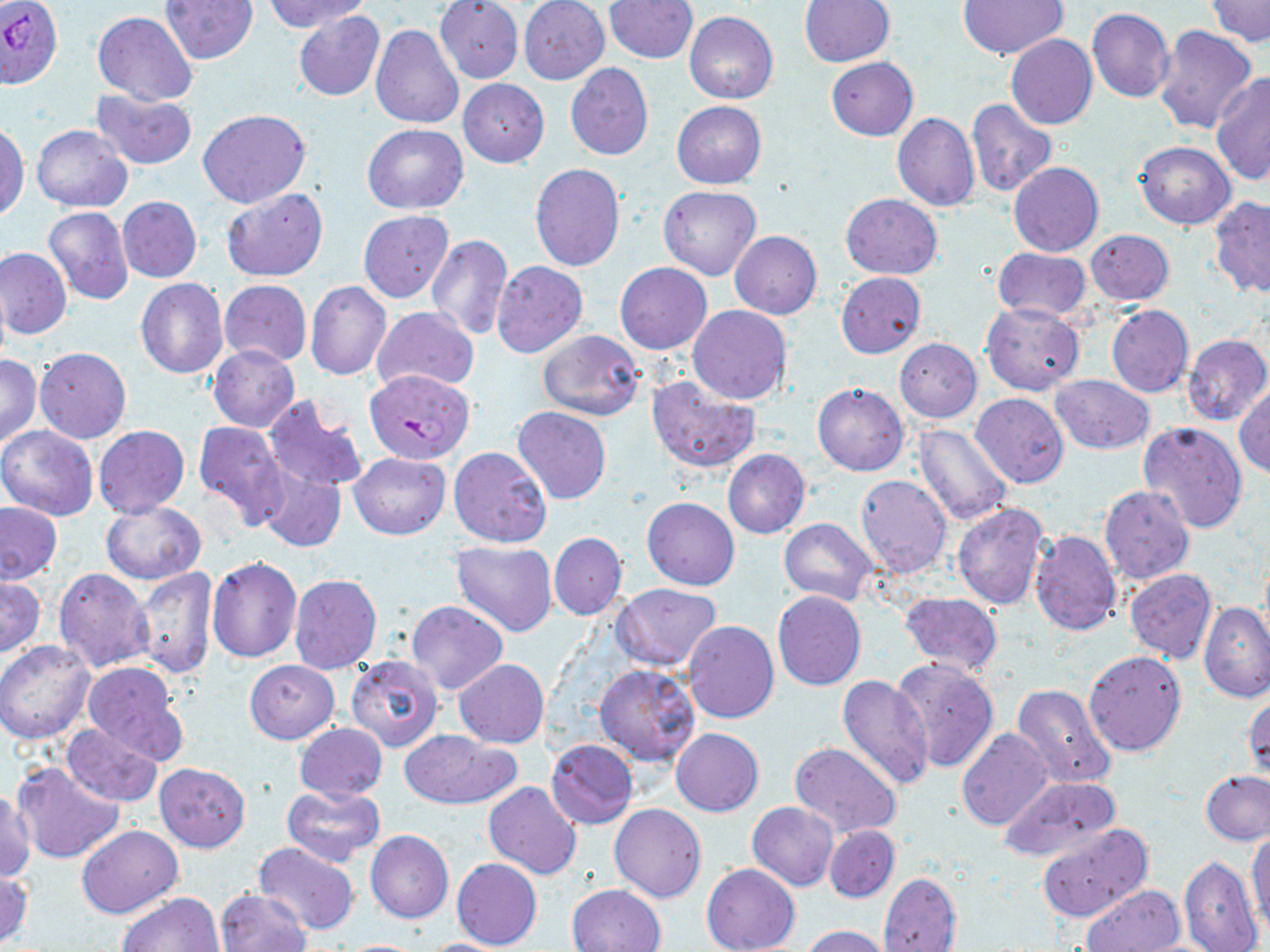 Approximate bounding boxes as (x1,y1)-(x2,y2) corner pairs in pixels. Uninfected red blood cell locations: (160,0)-(259,65), (605,0)-(698,63), (799,0)-(894,66), (1205,0)-(1270,46), (265,1)-(370,33), (518,1)-(609,85), (957,1)-(1067,59), (435,2)-(524,83), (1087,7)-(1175,103), (294,9)-(385,102), (92,12)-(197,105), (686,13)-(779,104), (371,25)-(463,127), (1154,25)-(1257,134), (1006,35)-(1097,130), (827,57)-(918,140), (565,63)-(653,161), (1211,73)-(1270,185), (458,79)-(550,167), (90,89)-(197,169), (966,100)-(1056,198), (672,101)-(765,188), (198,109)-(311,207), (893,112)-(979,212), (0,121)-(29,219), (31,124)-(132,212), (362,124)-(469,214), (1134,142)-(1235,229), (1009,163)-(1103,257), (530,164)-(625,271), (659,185)-(761,280), (221,187)-(328,281), (841,193)-(942,278), (118,196)-(202,282), (1210,196)-(1270,297), (43,207)-(134,306), (359,211)-(455,303), (729,230)-(822,319), (1085,230)-(1175,306), (426,235)-(514,342), (1,247)-(72,339), (993,247)-(1090,320), (492,260)-(588,359), (615,263)-(711,354), (836,271)-(926,358), (0,274)-(9,371), (137,278)-(228,378), (219,280)-(312,365), (305,280)-(392,380), (981,302)-(1085,395), (373,305)-(479,393), (687,305)-(791,404), (1106,305)-(1193,399), (537,329)-(644,422), (1182,334)-(1270,426), (895,338)-(982,422), (208,344)-(300,431), (36,347)-(130,444), (0,354)-(42,449), (1050,375)-(1154,454), (646,376)-(761,474), (813,383)-(909,476), (1235,385)-(1270,478), (972,392)-(1069,487), (263,396)-(366,496), (513,405)-(611,503), (194,420)-(288,526), (1138,421)-(1248,532), (911,423)-(1014,528), (93,425)-(189,518), (0,426)-(97,521), (449,446)-(552,547), (723,450)-(810,539), (349,452)-(451,539), (259,469)-(345,551), (855,475)-(953,578), (1100,485)-(1195,586), (643,497)-(740,590), (100,501)-(206,583), (0,502)-(63,584), (952,502)-(1050,611), (779,517)-(877,607), (1029,529)-(1122,636), (549,532)-(626,619), (450,542)-(558,637), (207,557)-(302,661), (131,566)-(218,680), (54,568)-(154,673), (1124,568)-(1217,663), (289,573)-(381,673), (0,576)-(45,658), (613,583)-(722,671), (772,590)-(867,690), (901,591)-(1003,675), (405,601)-(508,694), (1200,603)-(1270,701), (685,620)-(779,723), (1,640)-(96,744), (1084,651)-(1187,756), (345,655)-(443,753), (889,658)-(1000,775), (455,659)-(550,747), (81,660)-(190,764), (244,661)-(338,743), (594,663)-(700,766), (837,675)-(935,788), (1011,683)-(1117,790), (1243,690)-(1270,778), (60,723)-(163,805), (294,723)-(388,801), (671,728)-(764,816), (956,728)-(1053,833), (401,730)-(520,808), (547,739)-(638,828), (788,742)-(902,837), (11,761)-(125,867), (155,762)-(250,852), (1201,770)-(1270,843), (997,775)-(1122,866), (484,781)-(582,879), (281,783)-(386,866), (1,790)-(37,881), (747,802)-(839,890), (609,803)-(707,903), (1038,823)-(1153,923), (76,825)-(182,917), (824,825)-(898,902), (1248,828)-(1269,932), (367,831)-(454,924), (253,842)-(359,934), (1178,855)-(1262,952), (451,857)-(542,950), (702,864)-(800,952), (0,869)-(33,948), (879,872)-(961,952), (568,884)-(666,952), (1083,884)-(1184,951), (217,888)-(311,952), (117,892)-(224,952), (800,925)-(894,952), (414,938)-(513,951), (335,939)-(431,951). Plasmodium falciparum-infected red blood cell locations: (0,1)-(64,89), (366,370)-(474,465). Slide-level diagnosis: Plasmodium falciparum. Thin blood smear. Captured at 1000x magnification. May-Grünwald-Giemsa stain. Optical microscopy. Image is 1270×952 pixels. Single field of view.